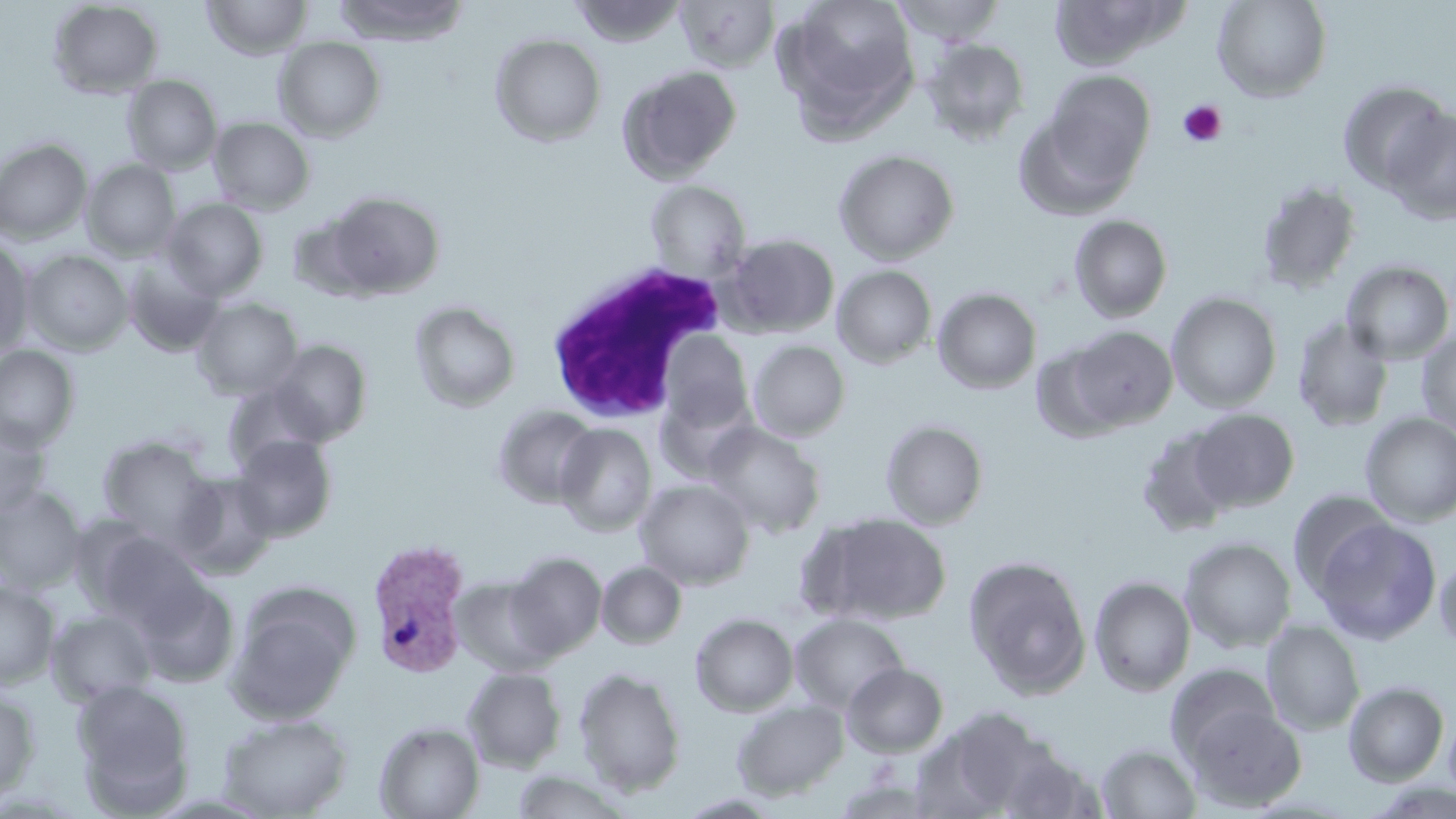
Approximate bounding boxes as (x1,y1)-(x2,y2) corner pairs in pixels. White blood cell locations: (543,261)-(733,422). Plasmodium vivax-infected red blood cell locations: (366,538)-(472,677). Platelet locations: (1178,100)-(1227,147). Uninfected red blood cell locations: (202,0)-(313,60), (333,0)-(470,45), (570,0)-(686,47), (675,0)-(779,72), (773,0)-(920,136), (890,0)-(1006,44), (1212,0)-(1331,101), (48,1)-(164,99), (1048,2)-(1184,71), (490,33)-(607,146), (273,37)-(386,142), (921,39)-(1030,146), (617,65)-(742,183), (1040,69)-(1156,185), (122,75)-(222,174), (1336,80)-(1451,193), (1014,105)-(1143,221), (1383,108)-(1456,225), (208,116)-(315,214), (0,138)-(93,244), (833,149)-(959,264), (81,159)-(181,260), (645,180)-(750,280), (1255,180)-(1362,294), (324,191)-(445,298), (162,198)-(268,299), (288,211)-(380,301), (1069,214)-(1173,322), (722,233)-(840,337), (0,238)-(35,356), (22,250)-(133,355), (122,257)-(223,357), (1341,260)-(1455,364), (832,265)-(937,368), (932,288)-(1042,394), (1166,292)-(1282,412), (191,298)-(303,400), (409,300)-(521,412), (1292,316)-(1395,432), (1067,325)-(1177,430), (1416,329)-(1456,437), (659,332)-(753,432), (748,339)-(850,441), (268,340)-(373,445), (0,345)-(80,451), (222,380)-(328,474), (654,391)-(756,483), (492,405)-(601,508), (1188,408)-(1299,512), (1359,412)-(1456,526), (0,416)-(53,517), (880,418)-(989,529), (702,422)-(827,538), (555,424)-(657,536), (1136,424)-(1240,537), (231,434)-(338,541), (98,437)-(213,544), (172,471)-(278,578), (634,479)-(755,590), (0,486)-(87,593), (1287,490)-(1396,598), (809,513)-(952,625), (1312,517)-(1441,644), (88,529)-(206,630), (1180,536)-(1297,653), (506,551)-(607,659), (1433,552)-(1456,654), (963,555)-(1092,698), (597,561)-(687,648), (133,575)-(240,687), (1089,575)-(1196,696), (452,576)-(555,676), (0,581)-(59,688), (227,596)-(356,725), (47,609)-(156,707), (690,613)-(799,717), (790,613)-(908,713), (1261,620)-(1365,735), (842,662)-(948,757), (1166,664)-(1280,765), (573,666)-(687,796), (462,667)-(567,772), (71,679)-(196,816), (1343,681)-(1450,786), (0,687)-(40,805), (731,700)-(848,800), (1184,701)-(1306,811), (917,706)-(1059,815), (1442,710)-(1456,806), (217,713)-(353,818), (375,721)-(484,819), (996,743)-(1104,818), (1097,744)-(1202,819), (509,770)-(632,818). Slide-level diagnosis: Plasmodium vivax. Image is 1456×819 pixels. Captured at 1000x magnification. One field of a larger specimen. Optical microscopy. Thin blood smear. May-Grünwald-Giemsa-stained preparation.